Classify this cell by malaria status.
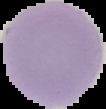
Uninfected.

Summary:
  - Preparation: thin blood film
  - Image type: cell region segmented out of the field of view; surrounding area masked to black
  - Image size: 106×109 pixels